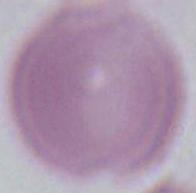

A red blood cell is shown. Captured at 1000x magnification. Micrograph.